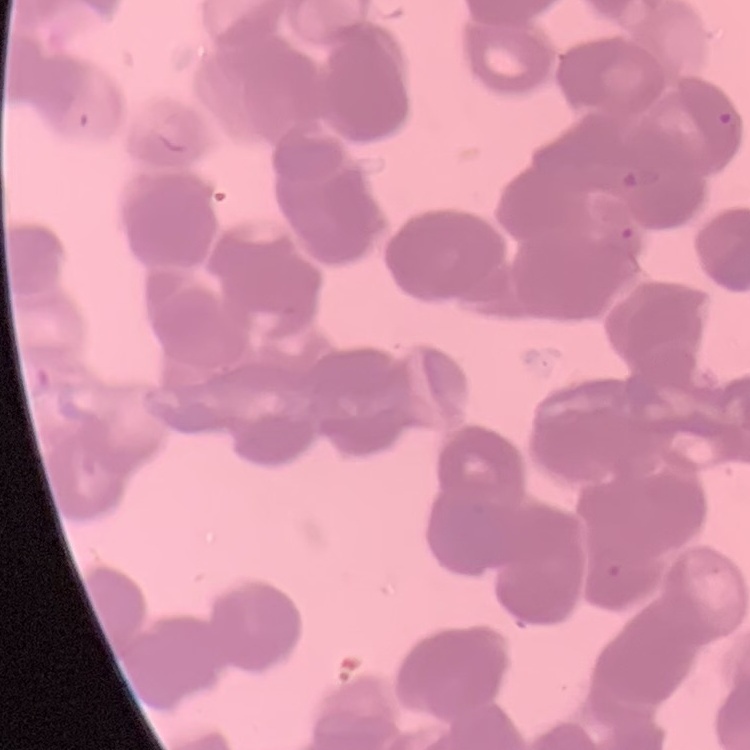

The erythrocytes exhibit rouleaux formation. One tile cut from a larger photomicrograph. Stained with either Field's or Giemsa. Thin blood smear.